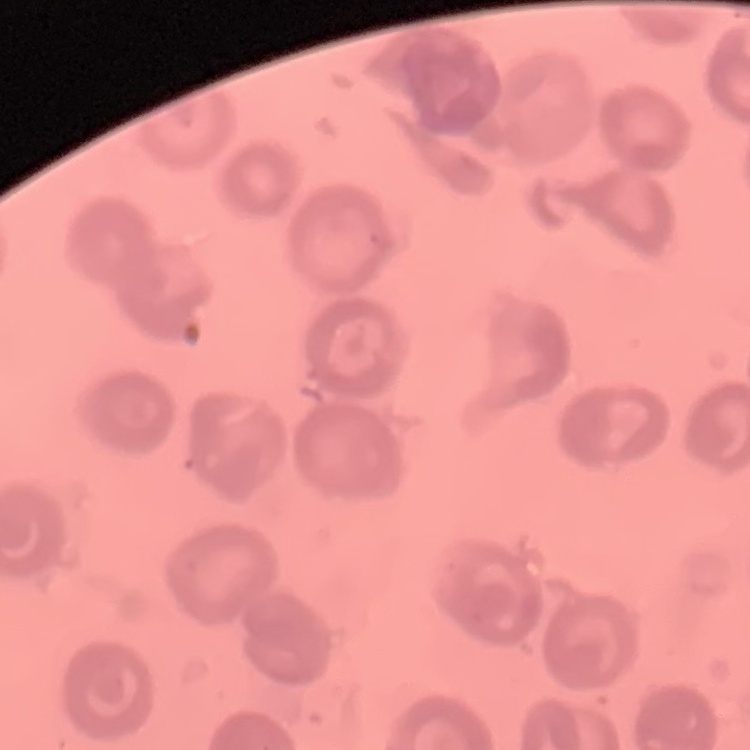

Summary:
  - Erythrocyte morphology: no rouleaux formation
  - Preparation: thin blood smear
  - Stain: Field's or Giemsa
  - Image type: square crop of a larger photomicrograph